Assess for Plasmodium parasites.
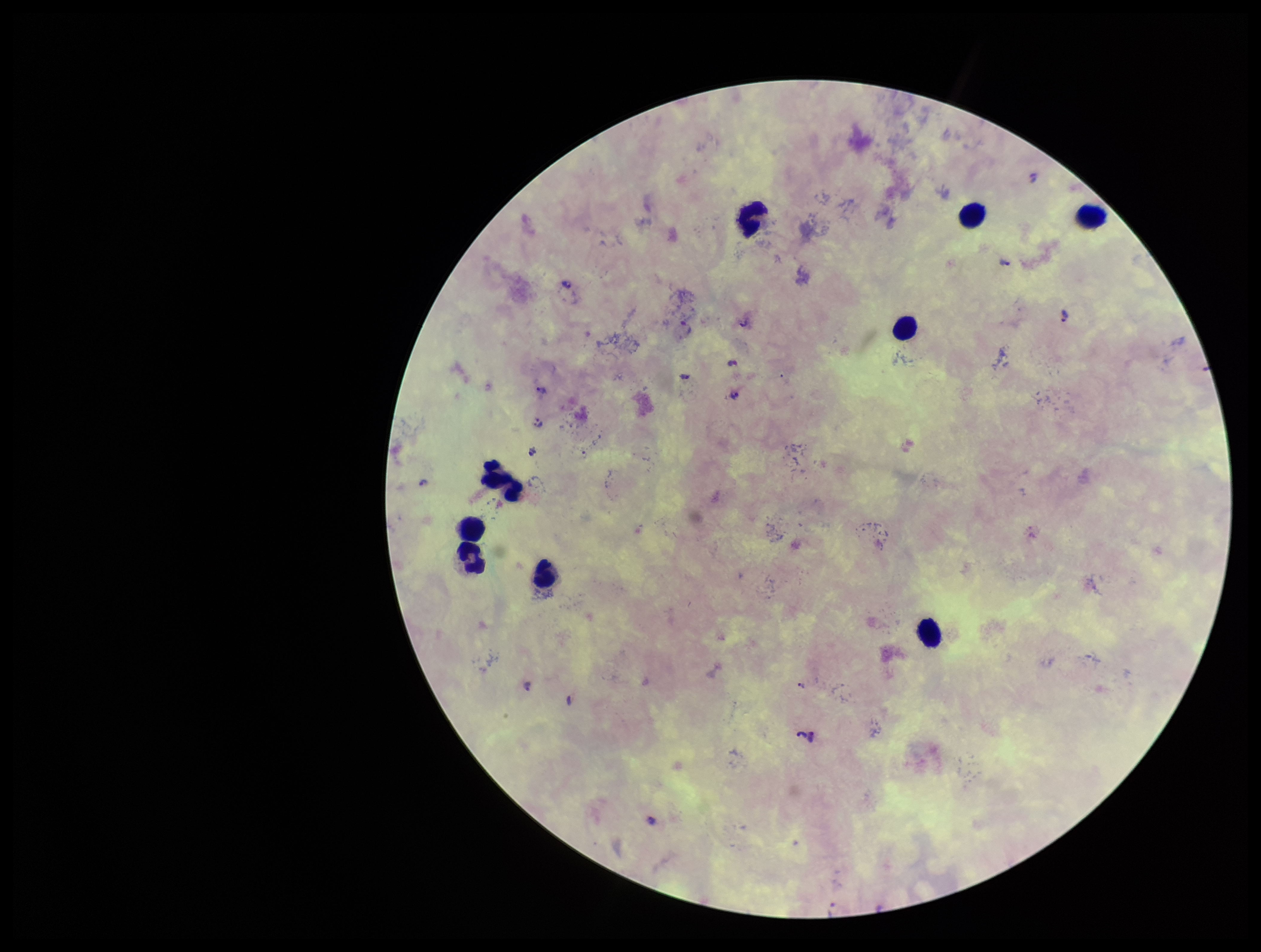
Identified.

Giemsa stain. Preparation: thick smear. Parasite count: 8. Image is 1261×952 pixels. Patient malaria status: infected. Leukocyte count: 9. Single field of view. Species reported for this patient: Plasmodium falciparum. Photographed through the microscope eyepiece with a smartphone camera.